Classify this cell by malaria status.
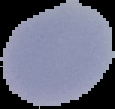
Uninfected.

The area outside the segmented cell region is set to black. From a thin blood film. Image is 115×109 pixels.